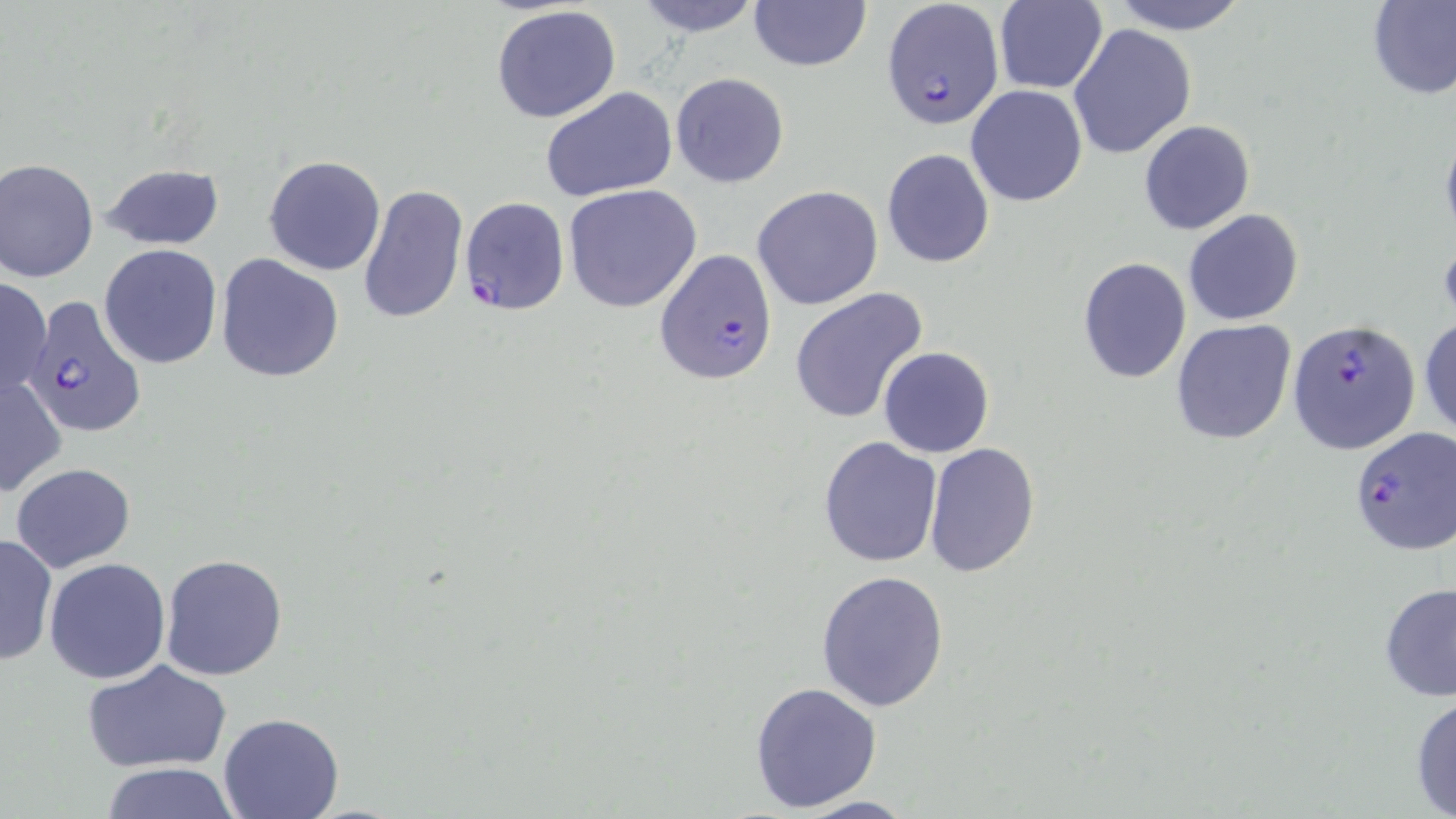

slide_level_diagnosis: Plasmodium falciparum
field_of_view: one of a larger specimen
modality: light microscopy
image_size: 1456×819 pixels
magnification: 1000x
plasmodium_falciparum_infected_red_blood_cell_locations: 'approximate bounding boxes as [x1, y1, x2, y2] in pixels: [880, 0, 1006, 131], [460, 196, 570, 316], [653, 248, 779, 386], [19, 295, 147, 437], [1290, 319, 1419, 455], [1351, 426, 1454, 556]'
preparation: thin blood film
uninfected_red_blood_cell_locations: 'approximate bounding boxes as [x1, y1, x2, y2] in pixels: [629, 0, 767, 38], [1106, 0, 1253, 35], [1367, 0, 1456, 102], [747, 1, 873, 73], [994, 1, 1107, 94], [491, 5, 622, 124], [1068, 23, 1198, 160], [669, 72, 791, 189], [965, 85, 1088, 207], [539, 87, 678, 202], [1138, 119, 1256, 235], [881, 148, 996, 268], [263, 154, 386, 276], [1, 158, 99, 283], [101, 163, 225, 251], [357, 182, 469, 326], [752, 184, 883, 311], [564, 186, 702, 313], [1183, 208, 1304, 325], [99, 244, 221, 368], [216, 254, 345, 382], [1077, 257, 1191, 384], [0, 276, 50, 400], [789, 288, 928, 424], [1418, 317, 1455, 442], [1170, 319, 1297, 446], [878, 345, 994, 458], [0, 375, 66, 497], [818, 437, 943, 570], [923, 442, 1039, 580], [10, 462, 138, 571], [0, 534, 56, 668], [160, 554, 288, 680], [43, 557, 172, 685], [815, 568, 949, 713], [1380, 580, 1456, 701], [83, 659, 231, 773], [747, 681, 882, 812], [1409, 692, 1456, 817], [218, 711, 343, 819], [96, 763, 244, 818], [785, 794, 924, 818]'
stain: May-Grünwald-Giemsa